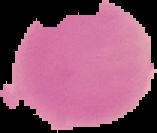

preparation = thin blood film
image type = segmented cell region with the area outside set to black
image size = 157×133 pixels
result = no malaria parasites seen